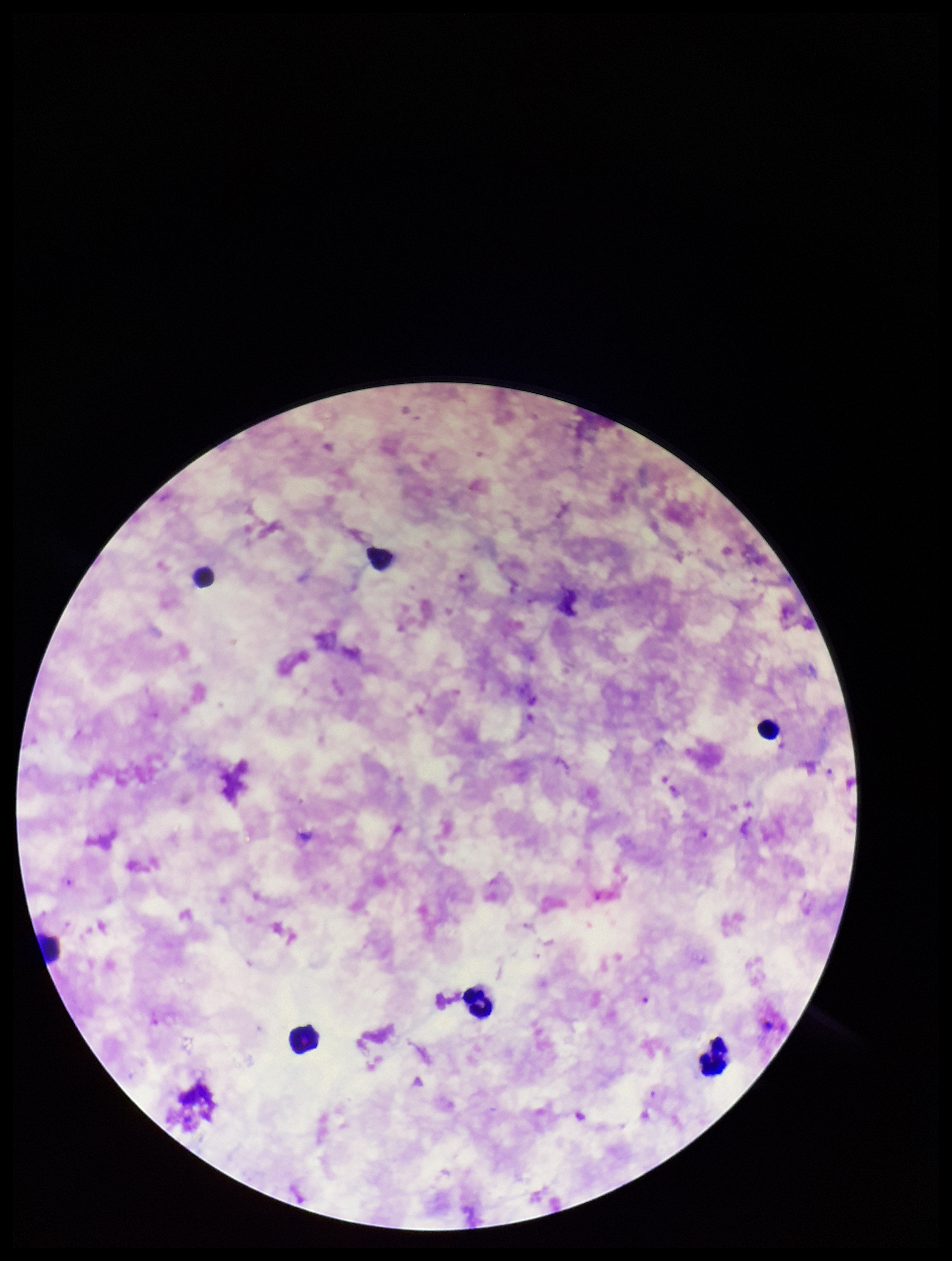
Summary:
  - Image size: 952×1261 pixels
  - Parasite count: 2
  - Capture: smartphone photograph through the microscope eyepiece
  - Field of view: single
  - Species reported for this patient: Plasmodium falciparum
  - Preparation: thick blood smear
  - Leukocyte count: 7
  - Stain: Giemsa
  - Patient malaria status: positive
  - Plasmodium parasites: identified